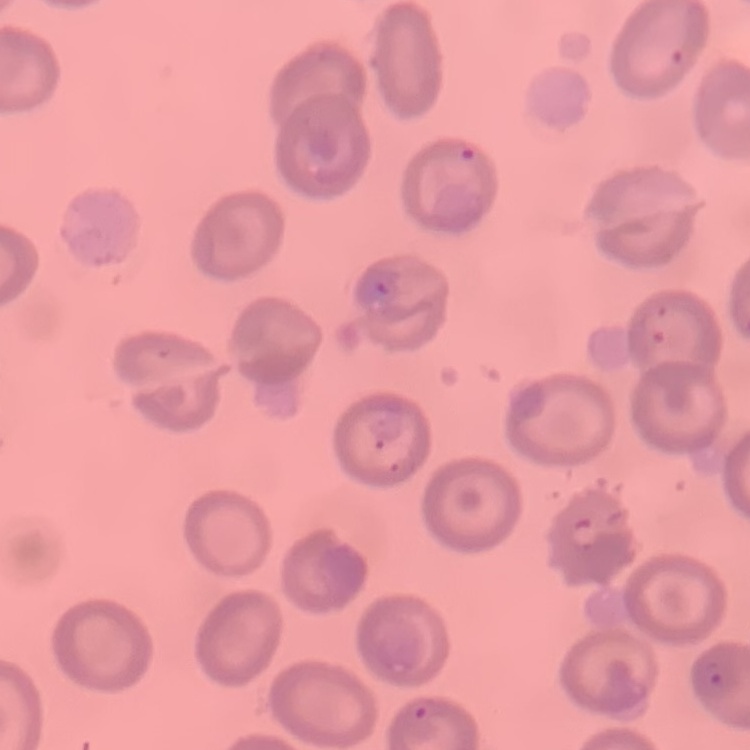
Summary:
  - Erythrocyte morphology: no rouleaux formation
  - Stain: Field's or Giemsa
  - Preparation: thin blood smear
  - Image type: one tile cut from a larger photomicrograph